Identify the blood parasite species.
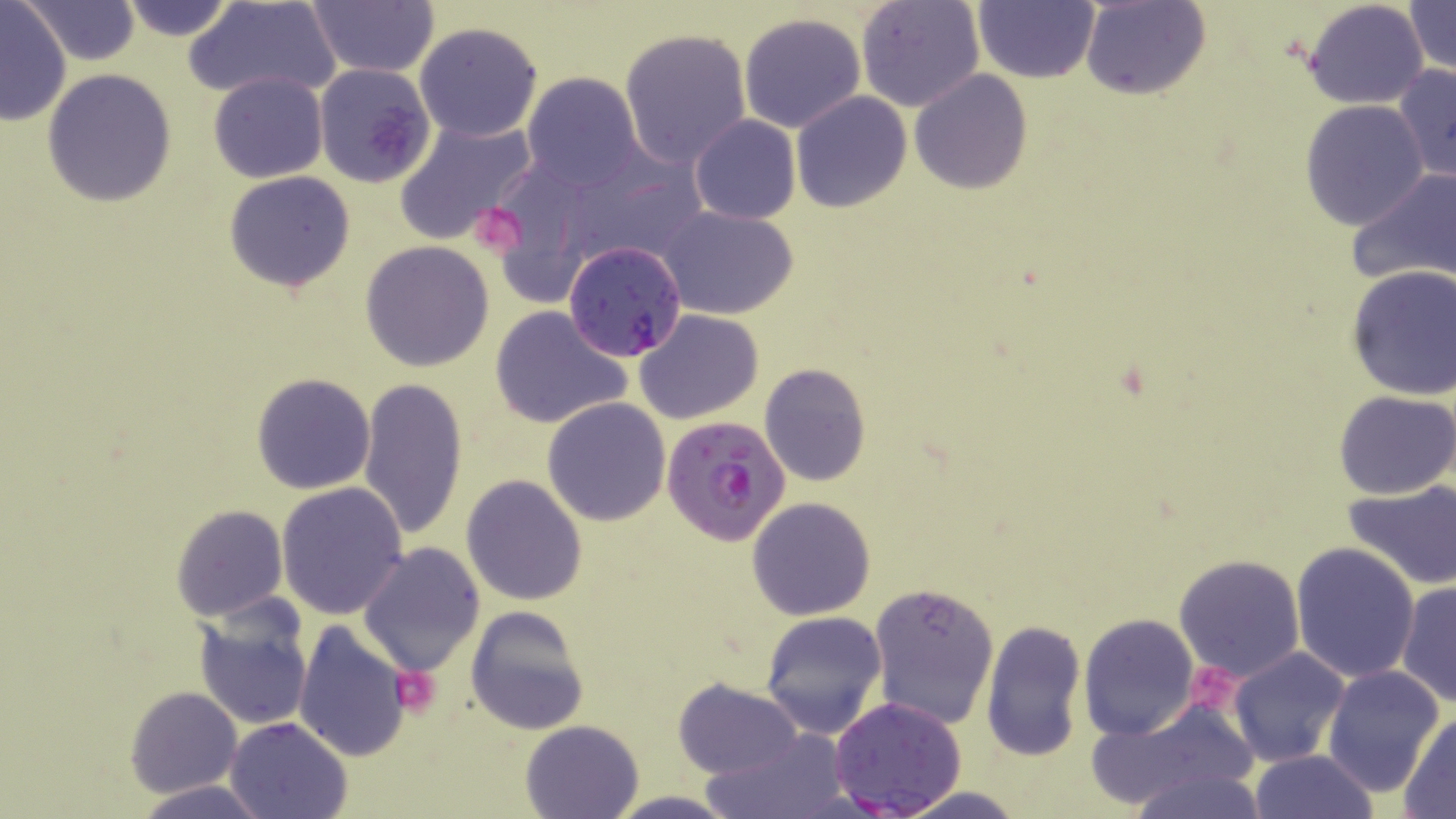
Plasmodium falciparum.

image size = 1456×819 pixels
uninfected red blood cell locations = approximate bounding boxes as (x1,y1)-(x2,y2) corner pairs in pixels: (114,0)-(241,42), (187,0)-(341,103), (856,0)-(984,112), (1082,0)-(1210,100), (1303,0)-(1430,110), (1404,0)-(1454,78), (26,1)-(141,64), (0,2)-(72,124), (306,2)-(438,79), (973,2)-(1100,84), (739,12)-(867,134), (414,21)-(544,142), (618,29)-(751,169), (873,35)-(1006,180), (313,64)-(435,188), (1393,64)-(1456,186), (42,69)-(177,207), (909,71)-(1033,193), (209,72)-(327,183), (521,72)-(643,190), (790,92)-(911,212), (1300,100)-(1429,230), (689,114)-(800,225), (395,115)-(538,246), (1348,166)-(1456,288), (224,170)-(357,292), (657,205)-(799,320), (359,241)-(494,371), (1345,266)-(1456,400), (489,305)-(631,429), (635,309)-(764,424), (759,363)-(871,488), (251,372)-(377,494), (358,376)-(468,540), (1333,390)-(1456,498), (541,397)-(671,525), (461,474)-(588,606), (1345,480)-(1456,590), (275,481)-(409,619), (746,496)-(876,621), (171,504)-(288,621), (359,543)-(484,677), (1291,543)-(1420,685), (1172,552)-(1306,683), (867,581)-(1001,729), (1396,582)-(1455,707), (192,597)-(315,733), (464,605)-(589,734), (761,611)-(888,739), (1079,613)-(1198,738), (980,619)-(1086,762), (294,620)-(414,763), (1227,647)-(1351,766), (1321,664)-(1445,797), (673,679)-(802,778), (125,685)-(243,798), (1085,699)-(1261,814), (1399,712)-(1456,816), (224,716)-(351,819), (520,719)-(645,818), (704,729)-(851,819), (1248,749)-(1381,819), (1129,765)-(1267,819), (131,780)-(272,818), (891,786)-(1032,818), (606,791)-(741,818)
Plasmodium falciparum-infected red blood cell locations = approximate bounding boxes as (x1,y1)-(x2,y2) corner pairs in pixels: (563,240)-(689,361), (661,411)-(789,546), (827,697)-(968,818)
magnification = 1000x
preparation = thin blood smear
platelet locations = approximate bounding boxes as (x1,y1)-(x2,y2) corner pairs in pixels: (468,202)-(531,261), (1190,661)-(1249,712), (390,665)-(441,718)
modality = light microscopy
stain = May-Grünwald-Giemsa
field of view = single